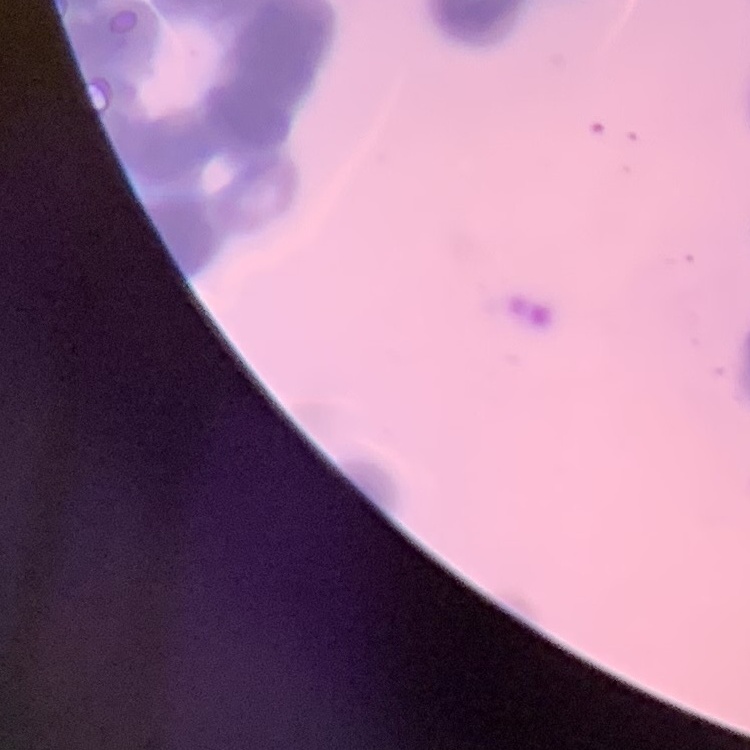

The red blood cells exhibit rouleaux formation. One tile cut from a larger photomicrograph. Thin blood smear. Stained with either Field's or Giemsa.